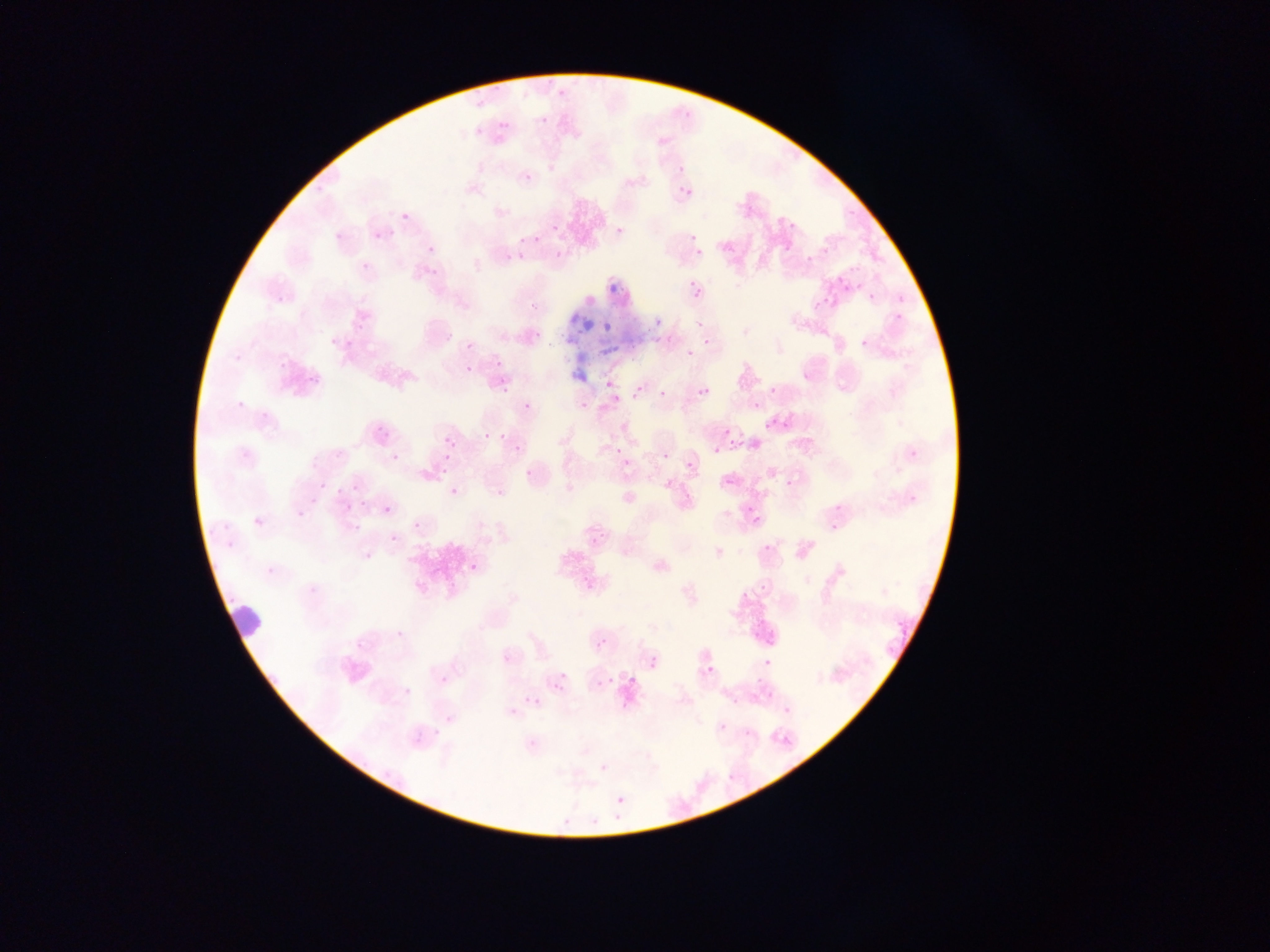

country = Ghana
leukocyte locations = approximate bounding boxes as (left, top, right, bottom) in pixels: (215, 595, 272, 644)
field of view = single
malaria parasite locations = approximate bounding boxes as (left, top, right, bottom) in pixels: (539, 116, 547, 124), (499, 121, 510, 131), (474, 128, 483, 136), (677, 166, 684, 174), (523, 172, 533, 183), (684, 187, 694, 197), (401, 213, 409, 220), (368, 221, 395, 247), (787, 221, 801, 231), (551, 224, 559, 232), (616, 227, 624, 235), (689, 233, 697, 242), (516, 237, 525, 246), (423, 239, 448, 256), (776, 246, 795, 267), (696, 248, 705, 256), (353, 257, 370, 270), (850, 264, 861, 273), (684, 277, 709, 301), (868, 294, 876, 302), (815, 300, 823, 309), (688, 316, 700, 325), (653, 317, 662, 325), (601, 322, 611, 332), (345, 339, 353, 348), (688, 339, 706, 354), (486, 357, 506, 373), (466, 366, 474, 374), (496, 380, 513, 399), (604, 381, 612, 389), (631, 385, 642, 399), (701, 386, 711, 395), (768, 387, 775, 395), (658, 390, 666, 398), (523, 392, 543, 416), (576, 395, 589, 415), (611, 395, 620, 404), (497, 414, 520, 457), (783, 421, 793, 429), (368, 423, 393, 454), (723, 429, 731, 437), (483, 433, 492, 441), (446, 436, 455, 446), (734, 439, 744, 448), (612, 445, 620, 453), (712, 446, 721, 454), (683, 451, 709, 472), (617, 452, 646, 479), (654, 454, 670, 471), (784, 478, 802, 488), (318, 481, 327, 490), (449, 487, 458, 495), (359, 501, 368, 511), (734, 503, 762, 516), (381, 504, 392, 515), (411, 520, 422, 531), (388, 534, 399, 544), (751, 547, 775, 556), (471, 563, 479, 572), (879, 588, 892, 600), (754, 590, 774, 599), (393, 609, 428, 645), (596, 639, 606, 649), (701, 651, 729, 673), (648, 659, 658, 668), (751, 661, 779, 680), (629, 674, 637, 684), (596, 678, 607, 688), (397, 683, 414, 693), (525, 695, 537, 707), (509, 706, 519, 716), (439, 718, 460, 737), (599, 763, 608, 773), (617, 795, 625, 803) | approximate (x, y) pixel centers of objects too small to bound: (443, 681)
capture = mobile-phone photograph through a microscope
preparation = thin blood film
image size = 1270×952 pixels